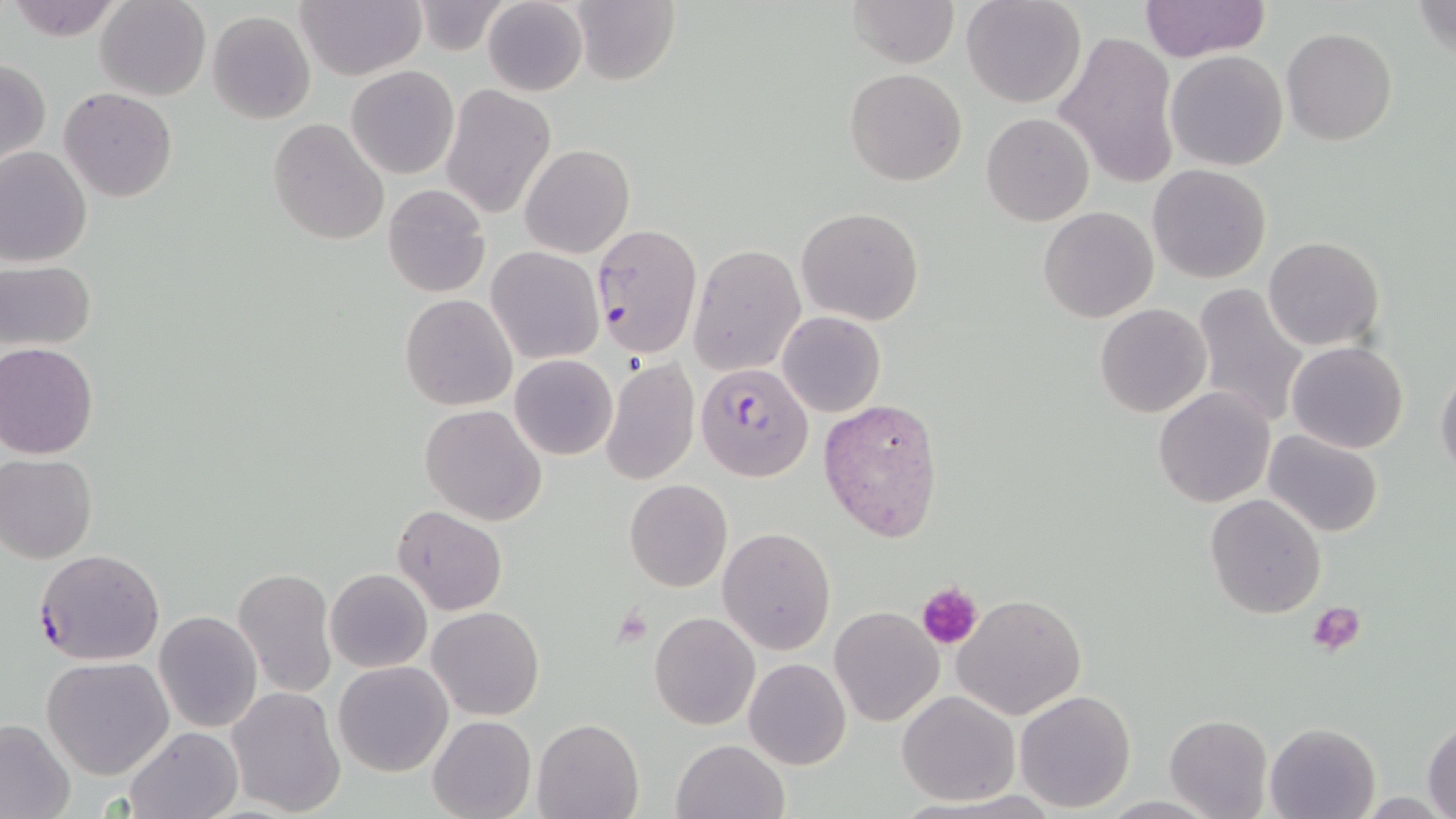

slide_level_diagnosis: Plasmodium falciparum
modality: light microscopy
plasmodium_falciparum_infected_red_blood_cell_locations: 'approximate bounding boxes as named x1/y1/x2/y2 corners in pixels: (x1=590, y1=222, x2=702, y2=359), (x1=695, y1=362, x2=813, y2=482), (x1=33, y1=548, x2=165, y2=665)'
stain: May-Grünwald-Giemsa
platelet_locations: 'approximate bounding boxes as named x1/y1/x2/y2 corners in pixels: (x1=918, y1=582, x2=982, y2=649), (x1=1311, y1=602, x2=1367, y2=655), (x1=610, y1=607, x2=654, y2=649)'
preparation: thin blood smear
magnification: 1000x
image_size: 1456×819 pixels
field_of_view: one of a larger specimen
uninfected_red_blood_cell_locations: 'approximate bounding boxes as named x1/y1/x2/y2 corners in pixels: (x1=5, y1=0, x2=124, y2=39), (x1=295, y1=0, x2=425, y2=80), (x1=481, y1=0, x2=588, y2=97), (x1=845, y1=0, x2=958, y2=67), (x1=962, y1=0, x2=1086, y2=109), (x1=1412, y1=0, x2=1456, y2=61), (x1=96, y1=1, x2=212, y2=101), (x1=570, y1=1, x2=679, y2=86), (x1=1138, y1=1, x2=1272, y2=61), (x1=410, y1=2, x2=510, y2=53), (x1=207, y1=11, x2=315, y2=125), (x1=1282, y1=28, x2=1398, y2=146), (x1=1054, y1=31, x2=1179, y2=188), (x1=1163, y1=39, x2=1403, y2=156), (x1=1165, y1=50, x2=1289, y2=170), (x1=1, y1=59, x2=49, y2=168), (x1=347, y1=65, x2=459, y2=179), (x1=844, y1=68, x2=966, y2=186), (x1=441, y1=85, x2=556, y2=219), (x1=60, y1=87, x2=177, y2=201), (x1=982, y1=114, x2=1094, y2=225), (x1=268, y1=117, x2=390, y2=246), (x1=0, y1=144, x2=93, y2=268), (x1=520, y1=144, x2=635, y2=257), (x1=1148, y1=164, x2=1272, y2=283), (x1=383, y1=184, x2=491, y2=299), (x1=796, y1=207, x2=924, y2=326), (x1=1039, y1=207, x2=1158, y2=324), (x1=1264, y1=236, x2=1384, y2=351), (x1=689, y1=244, x2=806, y2=377), (x1=487, y1=246, x2=603, y2=364), (x1=0, y1=260, x2=97, y2=351), (x1=1192, y1=282, x2=1309, y2=429), (x1=400, y1=294, x2=517, y2=410), (x1=1096, y1=304, x2=1212, y2=417), (x1=778, y1=311, x2=885, y2=417), (x1=1287, y1=340, x2=1408, y2=454), (x1=0, y1=342, x2=99, y2=459), (x1=509, y1=355, x2=617, y2=460), (x1=600, y1=359, x2=700, y2=485), (x1=1435, y1=366, x2=1456, y2=482), (x1=1152, y1=387, x2=1276, y2=508), (x1=818, y1=397, x2=945, y2=544), (x1=420, y1=404, x2=547, y2=527), (x1=1262, y1=430, x2=1384, y2=539), (x1=1, y1=454, x2=98, y2=563), (x1=624, y1=479, x2=732, y2=592), (x1=1205, y1=494, x2=1327, y2=620), (x1=393, y1=505, x2=507, y2=615), (x1=718, y1=527, x2=835, y2=654), (x1=233, y1=568, x2=337, y2=697), (x1=324, y1=569, x2=431, y2=673), (x1=953, y1=593, x2=1086, y2=721), (x1=427, y1=606, x2=543, y2=720), (x1=828, y1=606, x2=944, y2=728), (x1=154, y1=611, x2=261, y2=732), (x1=649, y1=611, x2=760, y2=730), (x1=41, y1=657, x2=173, y2=779), (x1=742, y1=658, x2=851, y2=770), (x1=334, y1=660, x2=454, y2=776), (x1=225, y1=687, x2=347, y2=817), (x1=1014, y1=690, x2=1137, y2=813), (x1=896, y1=691, x2=1019, y2=806), (x1=428, y1=715, x2=536, y2=819), (x1=1163, y1=715, x2=1272, y2=819), (x1=533, y1=717, x2=644, y2=819), (x1=0, y1=719, x2=75, y2=819), (x1=1424, y1=719, x2=1456, y2=816), (x1=1265, y1=722, x2=1383, y2=818), (x1=122, y1=728, x2=241, y2=818), (x1=671, y1=738, x2=788, y2=819)'